Locate and identify every blood parasite.
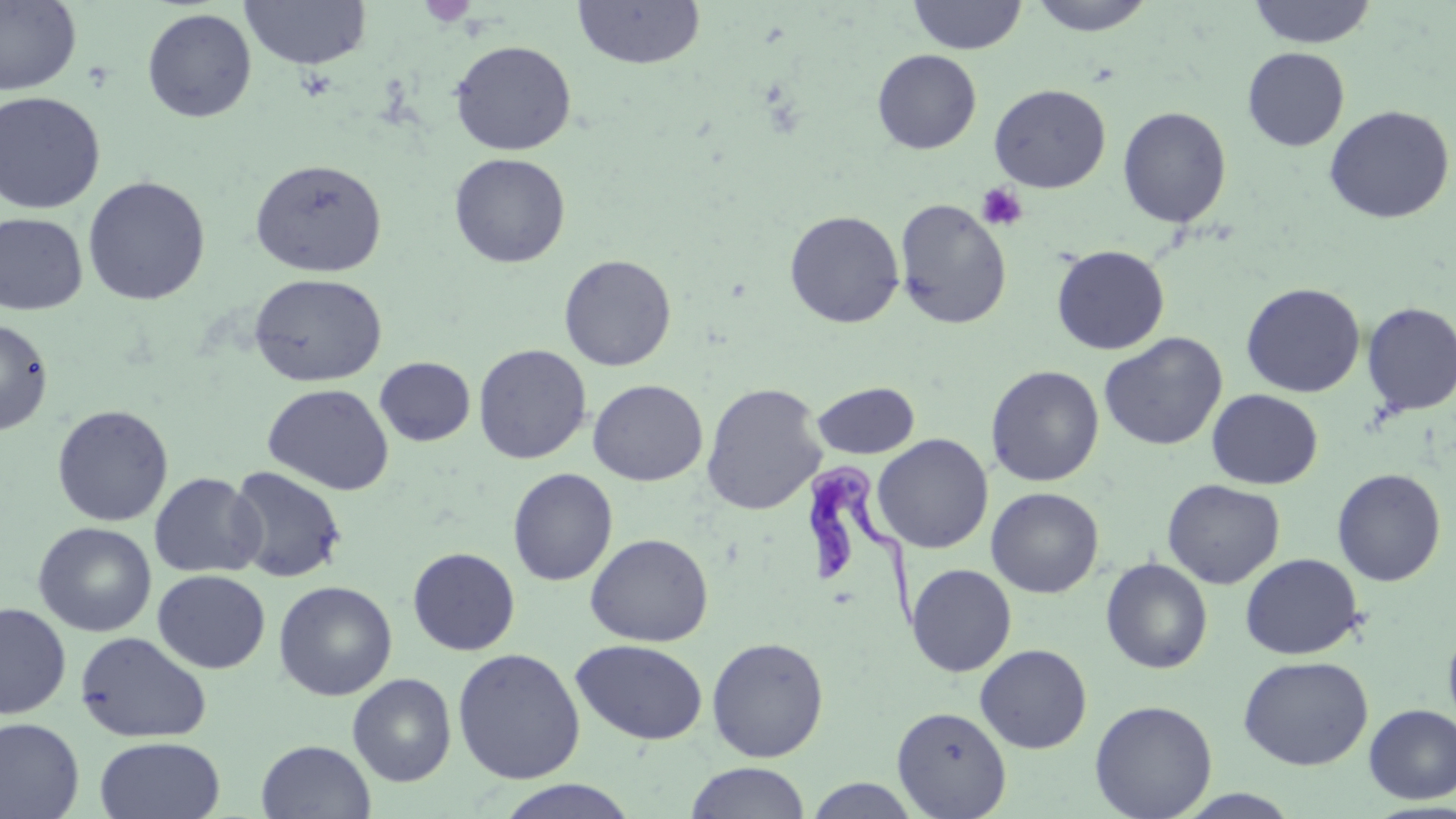
Approximate bounding boxes as named x1/y1/x2/y2 corners in pixels.
Trypanosoma brucei: (x1=799, y1=460, x2=928, y2=634).
No Plasmodium falciparum, Plasmodium ovale, Plasmodium malariae, Plasmodium vivax, or Babesia divergens observed.

Uninfected red blood cell locations: (x1=239, y1=0, x2=371, y2=70), (x1=571, y1=0, x2=706, y2=71), (x1=908, y1=0, x2=1028, y2=54), (x1=1027, y1=0, x2=1157, y2=36), (x1=1247, y1=0, x2=1377, y2=48), (x1=0, y1=1, x2=81, y2=95), (x1=142, y1=7, x2=257, y2=123), (x1=450, y1=40, x2=576, y2=156), (x1=1242, y1=47, x2=1349, y2=151), (x1=872, y1=49, x2=982, y2=154), (x1=989, y1=84, x2=1111, y2=193), (x1=0, y1=91, x2=106, y2=214), (x1=1324, y1=105, x2=1454, y2=224), (x1=1118, y1=106, x2=1232, y2=229), (x1=448, y1=153, x2=571, y2=268), (x1=250, y1=158, x2=387, y2=278), (x1=82, y1=175, x2=211, y2=306), (x1=894, y1=198, x2=1012, y2=330), (x1=784, y1=209, x2=904, y2=328), (x1=0, y1=213, x2=88, y2=315), (x1=1051, y1=244, x2=1170, y2=355), (x1=559, y1=254, x2=677, y2=371), (x1=249, y1=273, x2=387, y2=387), (x1=1241, y1=282, x2=1365, y2=398), (x1=1361, y1=302, x2=1456, y2=416), (x1=0, y1=317, x2=54, y2=436), (x1=1099, y1=332, x2=1227, y2=451), (x1=473, y1=343, x2=592, y2=464), (x1=375, y1=357, x2=475, y2=446), (x1=986, y1=365, x2=1104, y2=487), (x1=588, y1=379, x2=707, y2=486), (x1=812, y1=381, x2=919, y2=459), (x1=701, y1=382, x2=827, y2=515), (x1=262, y1=383, x2=394, y2=495), (x1=1207, y1=389, x2=1323, y2=489), (x1=51, y1=404, x2=173, y2=527), (x1=872, y1=434, x2=993, y2=554), (x1=226, y1=466, x2=347, y2=583), (x1=507, y1=467, x2=617, y2=586), (x1=1332, y1=468, x2=1446, y2=586), (x1=149, y1=472, x2=264, y2=578), (x1=1162, y1=478, x2=1285, y2=589), (x1=986, y1=487, x2=1104, y2=598), (x1=32, y1=521, x2=157, y2=637), (x1=585, y1=533, x2=713, y2=647), (x1=407, y1=547, x2=520, y2=655), (x1=1240, y1=553, x2=1364, y2=659), (x1=1100, y1=557, x2=1213, y2=674), (x1=906, y1=563, x2=1016, y2=676), (x1=153, y1=569, x2=270, y2=673), (x1=273, y1=580, x2=397, y2=701), (x1=0, y1=602, x2=71, y2=718), (x1=1443, y1=622, x2=1456, y2=737), (x1=75, y1=630, x2=212, y2=743), (x1=706, y1=636, x2=829, y2=762), (x1=570, y1=639, x2=707, y2=745), (x1=974, y1=644, x2=1092, y2=753), (x1=452, y1=647, x2=585, y2=785), (x1=1237, y1=655, x2=1374, y2=770), (x1=347, y1=673, x2=456, y2=787), (x1=1089, y1=699, x2=1218, y2=819), (x1=1363, y1=704, x2=1456, y2=803), (x1=891, y1=706, x2=1011, y2=818), (x1=0, y1=717, x2=85, y2=819), (x1=94, y1=736, x2=225, y2=819), (x1=256, y1=740, x2=375, y2=819), (x1=685, y1=762, x2=811, y2=819), (x1=804, y1=777, x2=923, y2=818), (x1=493, y1=779, x2=642, y2=819), (x1=1173, y1=789, x2=1304, y2=818). Platelet locations: (x1=418, y1=1, x2=478, y2=26), (x1=976, y1=183, x2=1028, y2=231). Slide-level diagnosis: Trypanosoma brucei. Image is 1456×819 pixels. May-Grünwald-Giemsa-stained preparation. Captured at 1000x magnification. Light microscopy. Single field of view. Thin blood film.